Locate every malaria parasite.
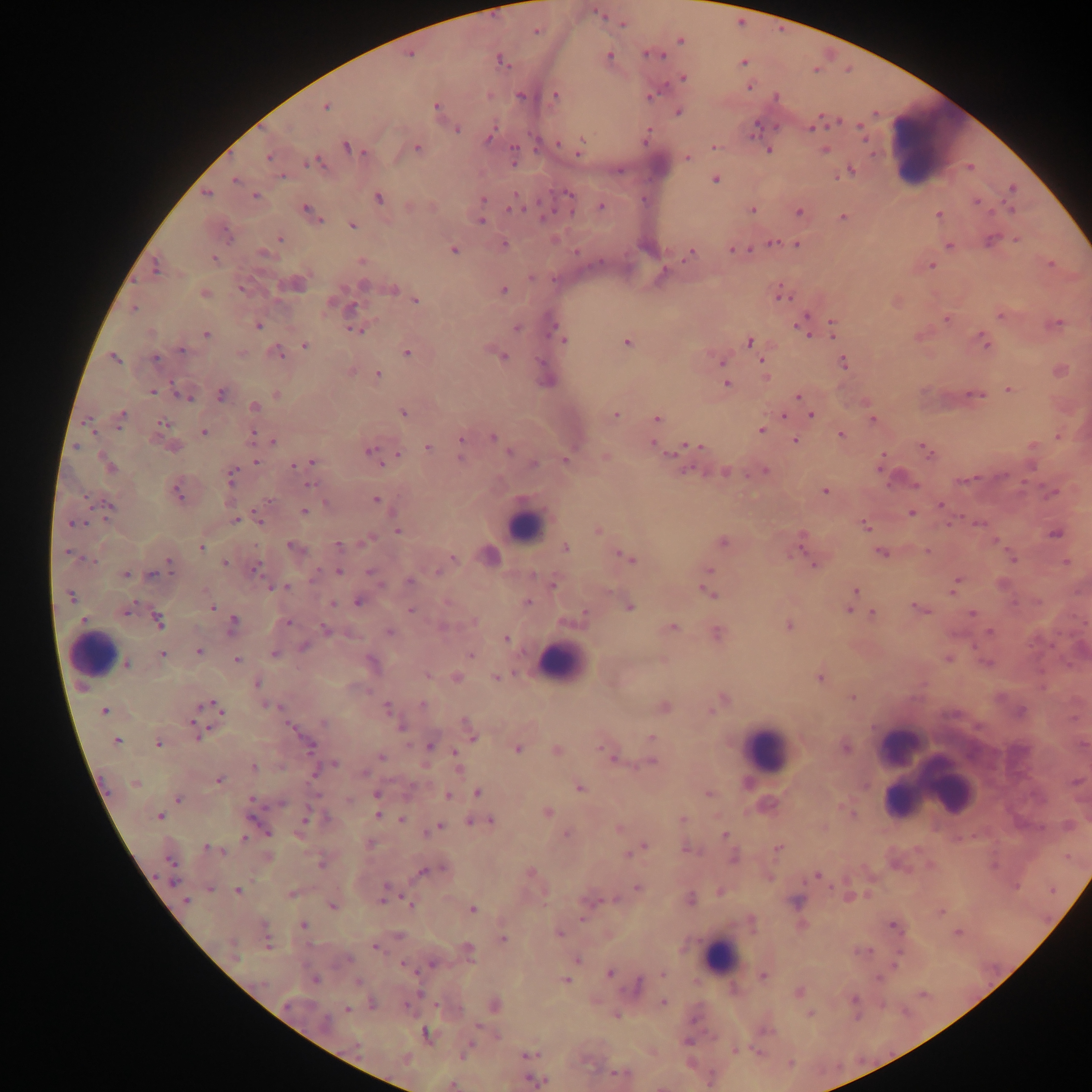

Approximate centers as [x, y] in pixels.
Malaria parasites: [623, 24], [537, 31], [680, 41], [650, 54], [609, 55], [410, 56], [501, 61], [743, 62], [683, 78], [749, 87], [555, 95], [650, 95], [520, 96], [326, 107], [436, 107], [678, 112], [457, 129], [811, 129], [489, 137], [581, 142], [560, 144], [347, 147], [713, 147], [417, 149], [580, 149], [514, 150], [768, 150], [824, 151], [268, 157], [687, 157], [311, 162], [513, 162], [850, 170], [283, 177], [235, 180], [715, 180], [1013, 189], [206, 194], [568, 194], [256, 196], [378, 199], [483, 199], [976, 202], [601, 206], [307, 208], [513, 208], [752, 211], [1011, 211], [799, 212], [311, 213], [939, 214], [843, 217], [319, 220], [481, 221], [353, 225], [279, 239], [1017, 240], [991, 241], [773, 243], [797, 244], [504, 245], [949, 246], [454, 249], [733, 250], [576, 252], [263, 253], [690, 254], [214, 260], [361, 261], [1051, 264], [931, 266], [156, 268], [531, 278], [295, 284], [364, 286], [393, 288], [241, 289], [504, 290], [205, 293], [783, 296], [416, 301], [133, 308], [352, 308], [1001, 315], [946, 319], [832, 322], [1057, 323], [259, 326], [516, 328], [555, 329], [804, 329], [355, 330], [206, 334], [561, 336], [984, 340], [627, 342], [750, 342], [305, 346], [182, 350], [279, 353], [407, 353], [241, 354], [503, 356], [114, 358], [155, 358], [540, 362], [722, 362], [761, 362], [843, 363], [378, 374], [546, 379], [727, 384], [1009, 389], [153, 392], [221, 394], [276, 395], [976, 395], [798, 396], [184, 397], [255, 406], [403, 412], [616, 415], [811, 415], [121, 416], [783, 416], [657, 418], [873, 419], [162, 422], [87, 423], [761, 430], [204, 432], [252, 434], [841, 436], [493, 437], [461, 439], [794, 440], [273, 442], [652, 445], [692, 445], [1032, 446], [173, 447], [427, 447], [370, 450], [925, 451], [508, 452], [398, 454], [460, 458], [605, 458], [566, 460], [256, 462], [313, 462], [534, 463], [293, 465], [108, 466], [1031, 466], [880, 467], [725, 472], [765, 472], [231, 475], [964, 480], [310, 484], [824, 491], [1053, 492], [177, 493], [376, 499], [941, 505], [109, 507], [304, 511], [911, 513], [236, 520], [260, 520], [73, 524], [978, 524], [865, 526], [599, 530], [397, 531], [1056, 534], [723, 543], [799, 544], [292, 546], [338, 546], [201, 547], [566, 547], [927, 552], [67, 553], [880, 553], [490, 556], [454, 558], [628, 558], [89, 560], [1012, 560], [170, 562], [1067, 562], [224, 564], [815, 565], [255, 569], [709, 571], [339, 572], [438, 572], [370, 573], [126, 574], [151, 574], [313, 579], [410, 581], [553, 583], [955, 585], [271, 587], [278, 587], [287, 588], [855, 591], [708, 592], [70, 596], [528, 601], [359, 602], [332, 604], [212, 607], [630, 608], [849, 608], [919, 608], [411, 609], [126, 611], [873, 613], [971, 614], [583, 615], [83, 620], [158, 620], [234, 622], [287, 622], [474, 622], [789, 626], [443, 627], [673, 628], [326, 630], [389, 632], [989, 632], [716, 633], [507, 639], [303, 646], [198, 651], [274, 654], [162, 655], [470, 655], [948, 659], [237, 660], [987, 662], [127, 663], [427, 676], [456, 677], [497, 677], [819, 677], [256, 684], [852, 697], [722, 700], [423, 704], [269, 705], [386, 706], [665, 707], [217, 708], [713, 710], [105, 711], [1021, 711], [324, 723], [194, 724], [467, 724], [290, 726], [400, 727], [471, 735], [197, 736], [651, 738], [116, 741], [158, 744], [310, 746], [430, 746], [846, 748], [518, 749], [557, 750], [455, 752], [605, 752], [382, 757], [614, 759], [652, 762], [333, 764], [254, 767], [364, 772], [219, 780], [135, 784], [579, 787], [478, 793], [709, 793], [377, 794], [448, 796], [178, 799], [251, 799], [348, 799], [282, 804], [547, 812], [378, 815], [159, 816], [305, 817], [683, 818], [402, 820], [490, 820], [470, 822], [438, 826], [619, 828], [432, 830], [268, 832], [567, 834], [725, 835], [244, 837], [645, 846], [209, 848], [777, 848], [690, 849], [217, 850], [629, 853], [734, 858], [169, 860], [321, 864], [441, 869], [422, 872], [530, 873], [817, 876], [174, 881], [638, 887], [210, 888], [387, 888], [237, 890], [291, 893], [384, 894], [691, 899], [383, 900], [611, 900], [186, 901], [796, 902], [411, 905], [333, 906], [472, 909], [892, 925], [304, 926], [559, 934], [958, 934], [399, 935], [503, 938], [267, 941], [231, 946], [375, 947], [468, 950], [866, 950], [349, 959], [577, 960], [432, 963], [404, 965], [610, 973], [662, 974], [763, 976], [879, 977], [315, 981], [566, 981], [357, 982], [638, 985], [799, 992], [855, 999], [663, 1003], [288, 1004], [373, 1004], [495, 1005], [405, 1006], [347, 1010], [810, 1015], [325, 1022], [426, 1033], [687, 1042], [356, 1046], [735, 1050], [465, 1053], [528, 1055], [621, 1073], [533, 1081], [452, 1085].

Summary:
  - Leukocyte locations: [934, 144], [524, 526], [93, 654], [560, 662], [901, 745], [766, 749], [909, 757], [930, 777], [947, 785], [901, 798], [720, 956]
  - Field of view: single
  - Capture: mobile-phone photograph through a microscope
  - Preparation: thick blood smear
  - Country: Ghana
  - Image size: 1092×1092 pixels